Assess the morphology of the red blood cells.
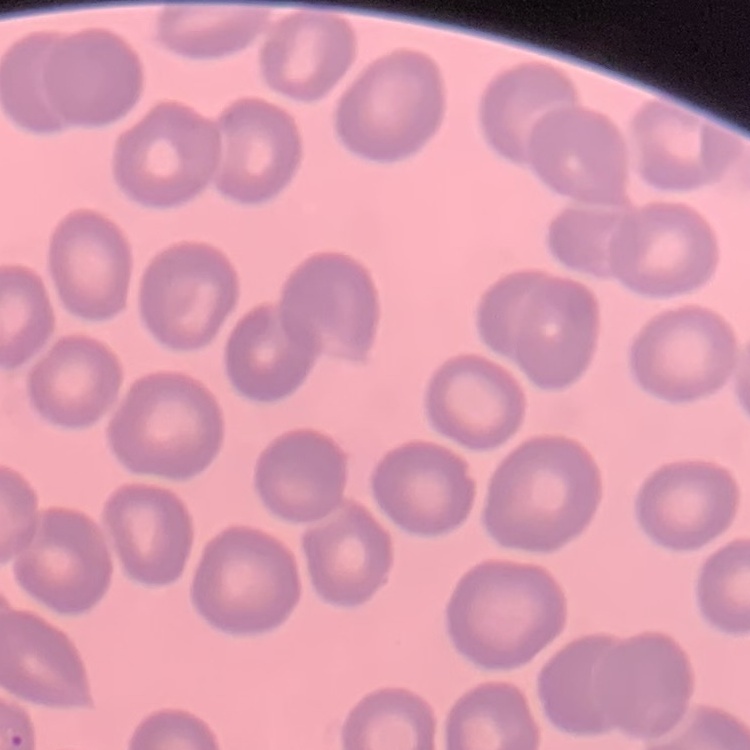
No rouleaux formation.

Summary:
  - Image type: one tile cut from a larger photomicrograph
  - Preparation: thin blood smear
  - Stain: Field's or Giemsa